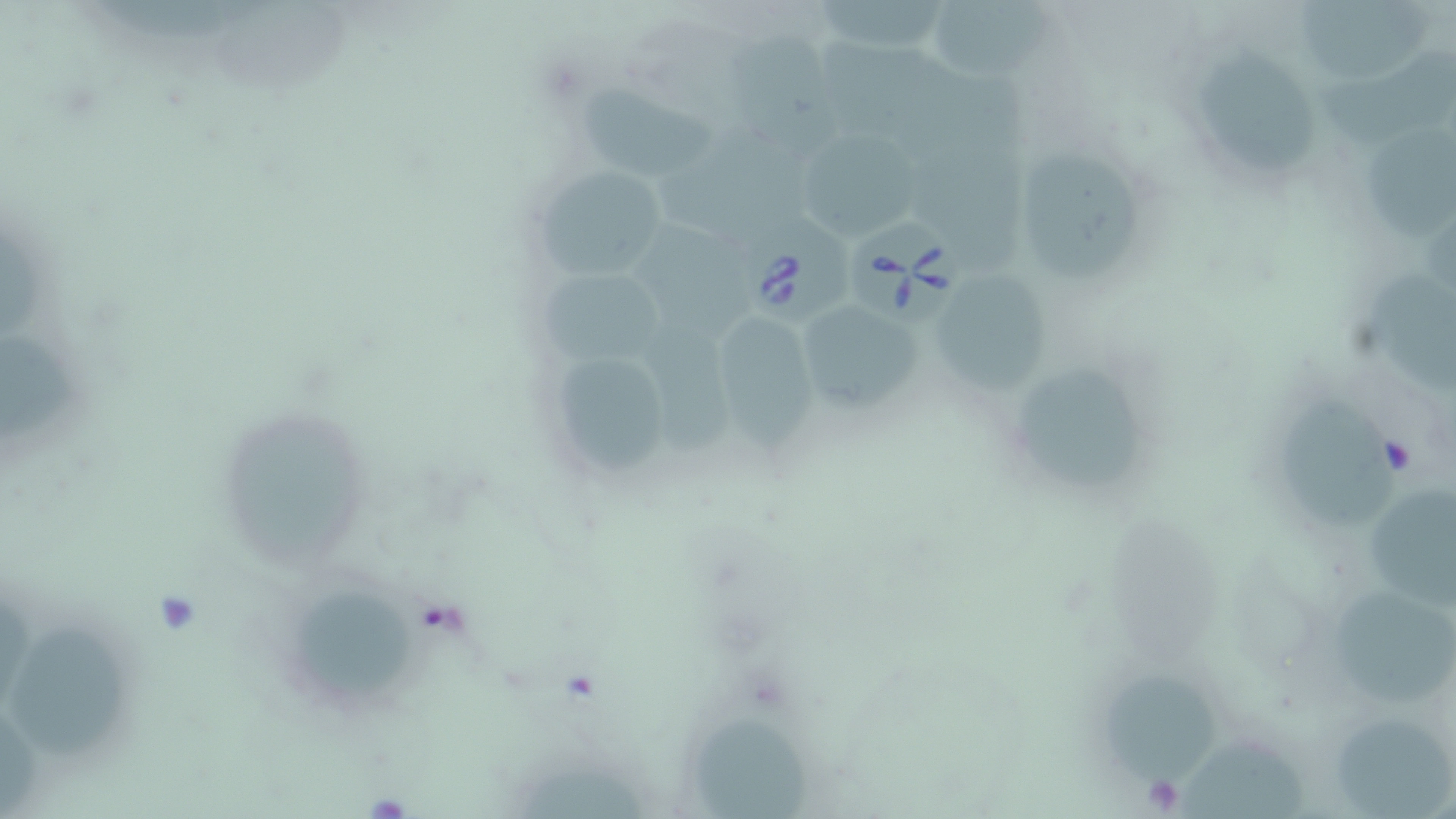

slide-level diagnosis = Babesia divergens
stain = May-Grünwald-Giemsa
Babesia divergens-infected red blood cell locations = approximate bounding boxes as [x1, y1, x2, y2] in pixels: [733, 210, 864, 327], [849, 219, 968, 330]
uninfected red blood cell locations = approximate bounding boxes as [x1, y1, x2, y2] in pixels: [814, 0, 950, 56], [928, 0, 1059, 80], [1291, 0, 1437, 80], [725, 37, 851, 164], [1314, 43, 1456, 145], [1200, 56, 1318, 176], [580, 84, 709, 177], [1365, 130, 1456, 237], [799, 134, 925, 237], [1023, 155, 1136, 280], [531, 163, 675, 278], [642, 220, 755, 350], [540, 264, 673, 363], [1365, 269, 1456, 395], [934, 272, 1058, 394], [807, 304, 928, 410], [724, 320, 819, 449], [645, 326, 751, 462], [0, 332, 78, 441], [552, 347, 677, 479], [1026, 369, 1142, 492], [1279, 393, 1400, 523], [235, 416, 381, 572], [1371, 489, 1456, 614], [1323, 590, 1455, 702], [300, 595, 413, 698], [11, 622, 129, 766], [1105, 672, 1224, 791], [693, 716, 812, 819], [1337, 721, 1455, 819], [1174, 737, 1307, 819]
image size = 1456×819 pixels
preparation = thin blood smear
modality = optical microscopy
field of view = one of a larger specimen
magnification = 1000x